Comment on the morphology of the erythrocytes.
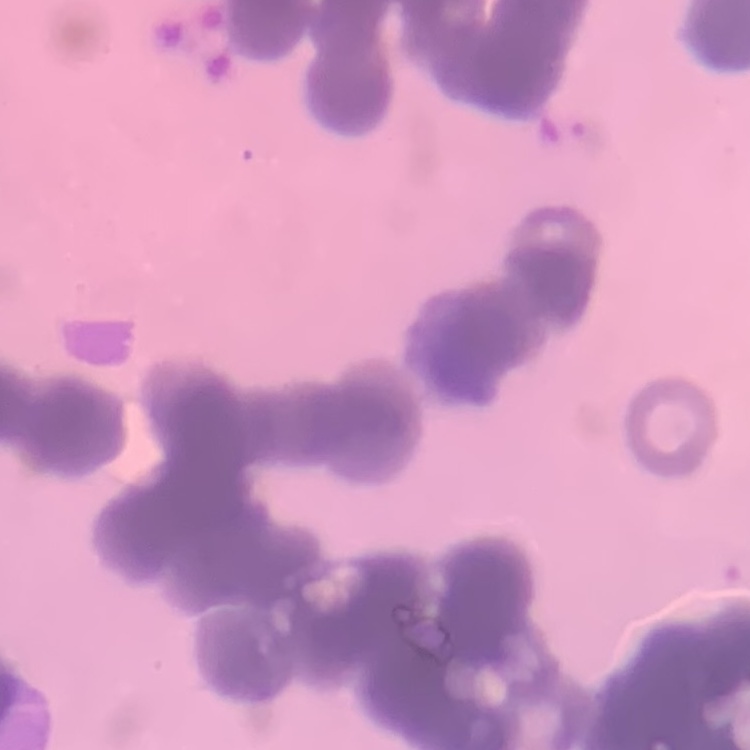

They show rouleaux formation.

image type = one tile cut from a larger photomicrograph
stain = Field's or Giemsa
preparation = thin blood film